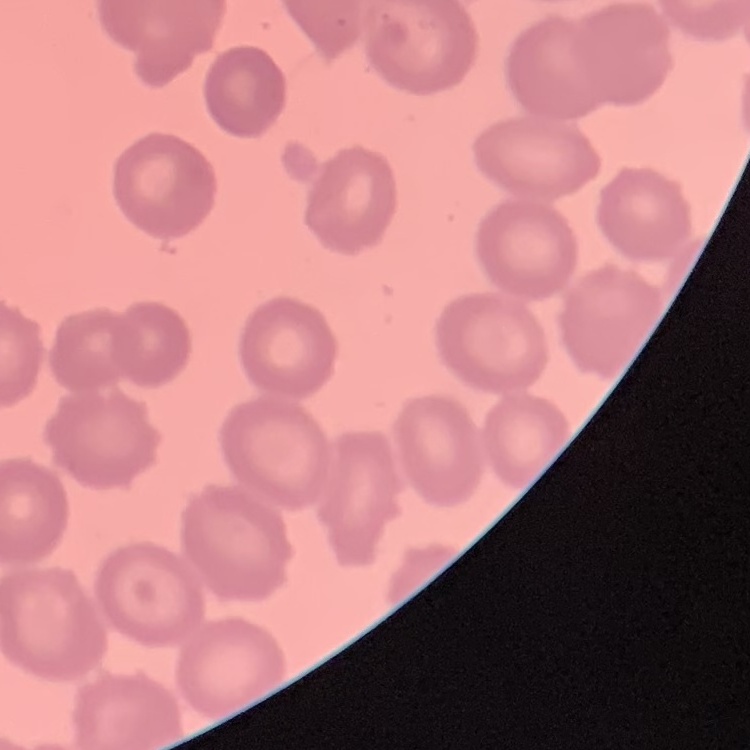

The red blood cells exhibit no rouleaux formation. Square crop of a larger photomicrograph. Thin blood smear. Stained with either Field's or Giemsa.